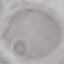

Result: no malaria parasites seen. Thin blood smear. Cell patch, automatically extracted from a larger field of view and resized to 64 × 64 pixels. Acquired by smartphone through the microscope eyepiece. Giemsa-stained preparation.